Assess this cell for malaria.
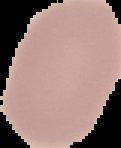

It is uninfected.

image size = 121×148 pixels
image type = cell region segmented out of the field of view; surrounding area masked to black
preparation = thin blood film